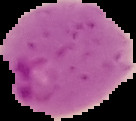
Image is 136×121 pixels. Malaria status: parasitized. From a thin blood smear. Segmented cell region on a black background.